Name the parasite shown.
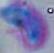

This is Toxoplasma gondii.

Summary:
  - Magnification: 1000x
  - Modality: micrograph